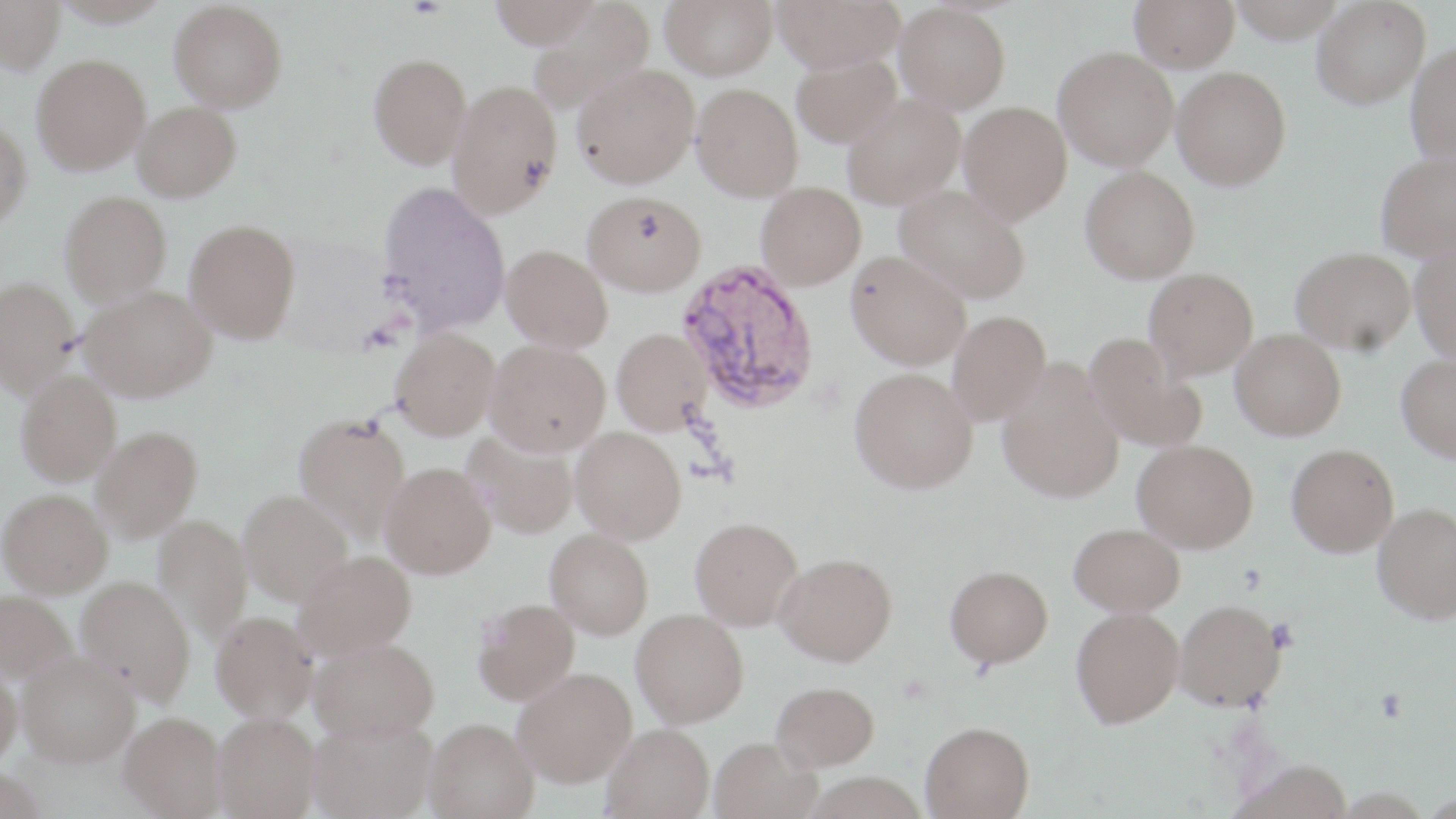

Approximate bounding boxes as named x1/y1/x2/y2 corners in pixels. Plasmodium vivax-infected red blood cell locations: (x1=675, y1=259, x2=821, y2=414). Uninfected red blood cell locations: (x1=488, y1=0, x2=605, y2=48), (x1=661, y1=0, x2=778, y2=80), (x1=772, y1=0, x2=905, y2=72), (x1=1130, y1=0, x2=1239, y2=71), (x1=1228, y1=0, x2=1348, y2=42), (x1=1312, y1=0, x2=1430, y2=109), (x1=0, y1=1, x2=64, y2=74), (x1=169, y1=1, x2=288, y2=112), (x1=528, y1=3, x2=656, y2=115), (x1=895, y1=3, x2=1011, y2=113), (x1=1406, y1=40, x2=1456, y2=166), (x1=1054, y1=46, x2=1179, y2=170), (x1=791, y1=52, x2=902, y2=148), (x1=32, y1=54, x2=150, y2=174), (x1=369, y1=54, x2=471, y2=169), (x1=572, y1=63, x2=699, y2=188), (x1=1172, y1=65, x2=1290, y2=189), (x1=448, y1=78, x2=562, y2=218), (x1=691, y1=83, x2=803, y2=201), (x1=842, y1=93, x2=965, y2=209), (x1=133, y1=101, x2=242, y2=201), (x1=959, y1=101, x2=1072, y2=223), (x1=0, y1=118, x2=32, y2=228), (x1=1375, y1=151, x2=1456, y2=260), (x1=1081, y1=166, x2=1200, y2=283), (x1=377, y1=181, x2=511, y2=333), (x1=756, y1=182, x2=866, y2=289), (x1=895, y1=185, x2=1031, y2=303), (x1=60, y1=190, x2=172, y2=305), (x1=583, y1=190, x2=707, y2=296), (x1=185, y1=218, x2=301, y2=343), (x1=1410, y1=241, x2=1456, y2=361), (x1=502, y1=244, x2=613, y2=351), (x1=1292, y1=247, x2=1416, y2=354), (x1=846, y1=250, x2=971, y2=369), (x1=1144, y1=268, x2=1258, y2=378), (x1=0, y1=276, x2=80, y2=396), (x1=80, y1=284, x2=216, y2=401), (x1=948, y1=310, x2=1051, y2=424), (x1=391, y1=328, x2=500, y2=440), (x1=612, y1=328, x2=712, y2=435), (x1=1230, y1=328, x2=1346, y2=440), (x1=1086, y1=334, x2=1208, y2=452), (x1=485, y1=339, x2=610, y2=455), (x1=1397, y1=354, x2=1456, y2=462), (x1=997, y1=361, x2=1124, y2=503), (x1=850, y1=367, x2=978, y2=493), (x1=16, y1=370, x2=121, y2=484), (x1=293, y1=413, x2=411, y2=539), (x1=91, y1=426, x2=202, y2=540), (x1=571, y1=426, x2=687, y2=543), (x1=463, y1=431, x2=579, y2=539), (x1=1133, y1=439, x2=1258, y2=552), (x1=1287, y1=444, x2=1399, y2=556), (x1=380, y1=462, x2=496, y2=578), (x1=0, y1=488, x2=112, y2=596), (x1=238, y1=489, x2=352, y2=605), (x1=1373, y1=502, x2=1456, y2=623), (x1=153, y1=514, x2=252, y2=643), (x1=690, y1=517, x2=803, y2=630), (x1=1070, y1=523, x2=1185, y2=616), (x1=545, y1=528, x2=654, y2=639), (x1=295, y1=551, x2=416, y2=659), (x1=774, y1=552, x2=897, y2=665), (x1=945, y1=565, x2=1053, y2=668), (x1=76, y1=576, x2=195, y2=703), (x1=0, y1=590, x2=77, y2=685), (x1=473, y1=598, x2=580, y2=704), (x1=1174, y1=599, x2=1286, y2=710), (x1=1071, y1=607, x2=1184, y2=727), (x1=631, y1=609, x2=749, y2=727), (x1=211, y1=611, x2=317, y2=721), (x1=310, y1=637, x2=438, y2=740), (x1=16, y1=651, x2=140, y2=766), (x1=0, y1=660, x2=23, y2=768), (x1=514, y1=667, x2=637, y2=786), (x1=772, y1=681, x2=879, y2=772), (x1=120, y1=711, x2=226, y2=817), (x1=213, y1=713, x2=320, y2=819), (x1=309, y1=717, x2=437, y2=819), (x1=425, y1=717, x2=538, y2=818), (x1=921, y1=721, x2=1035, y2=818), (x1=603, y1=723, x2=715, y2=819), (x1=710, y1=737, x2=822, y2=819), (x1=1231, y1=760, x2=1353, y2=819), (x1=0, y1=767, x2=48, y2=819). Slide-level diagnosis: Plasmodium vivax. 1000x magnification. May-Grünwald-Giemsa-stained preparation. Image is 1456×819 pixels. Thin blood film. Optical microscopy. Single field of view.